Point out each Plasmodium parasite.
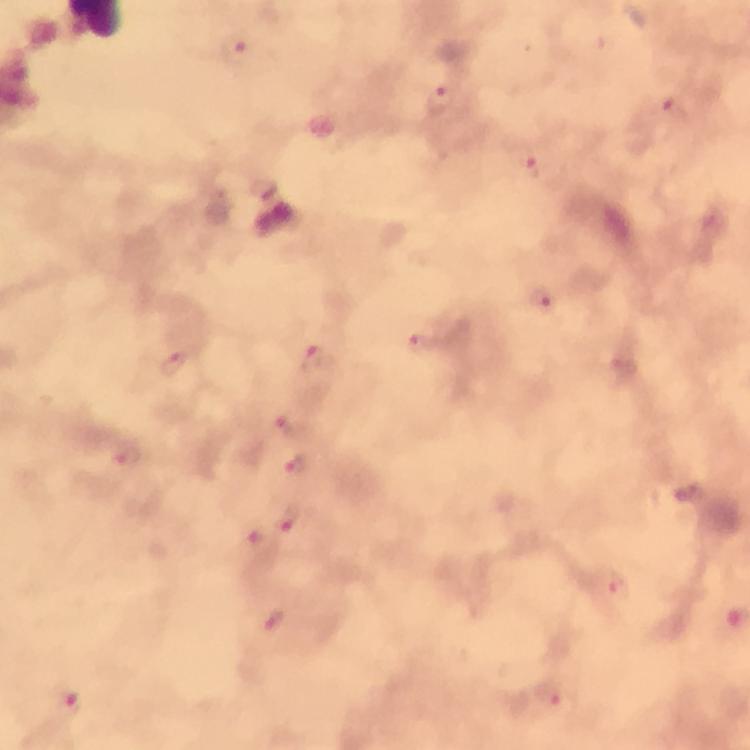

Approximate centers as (x, y) in pixels.
Plasmodium parasites: (240, 48), (443, 100), (676, 111), (533, 166), (544, 301), (426, 346), (313, 358), (177, 364), (291, 425), (131, 459), (299, 468), (290, 518), (251, 542), (619, 584), (556, 698), (72, 702).

immersion_oil: used
stain: Giemsa
capture: smartphone camera through the microscope
context: from a malaria diagnostic workup
magnification: 100x
preparation: thick blood smear
cropped_from: a single field of view
image_size: 750×750 pixels